State which parasite is depicted.
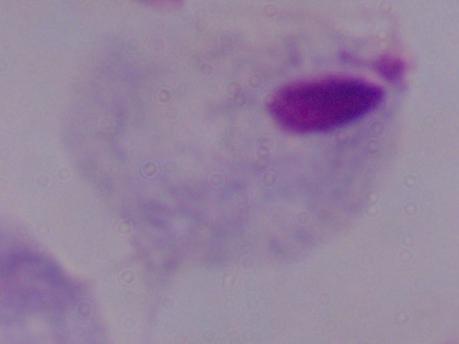

A trichomonad.

magnification = 1000x
modality = photomicrograph